State which parasite is depicted.
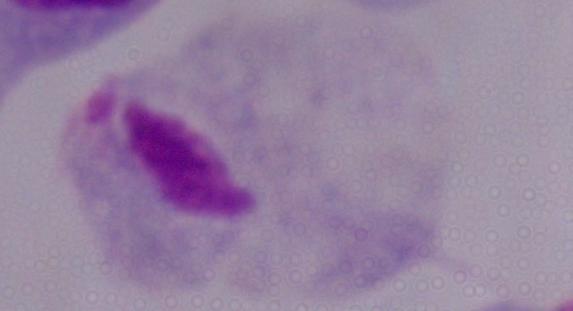
A trichomonad.

Summary:
  - Magnification: 1000x
  - Modality: micrograph